Identify the preparation type.
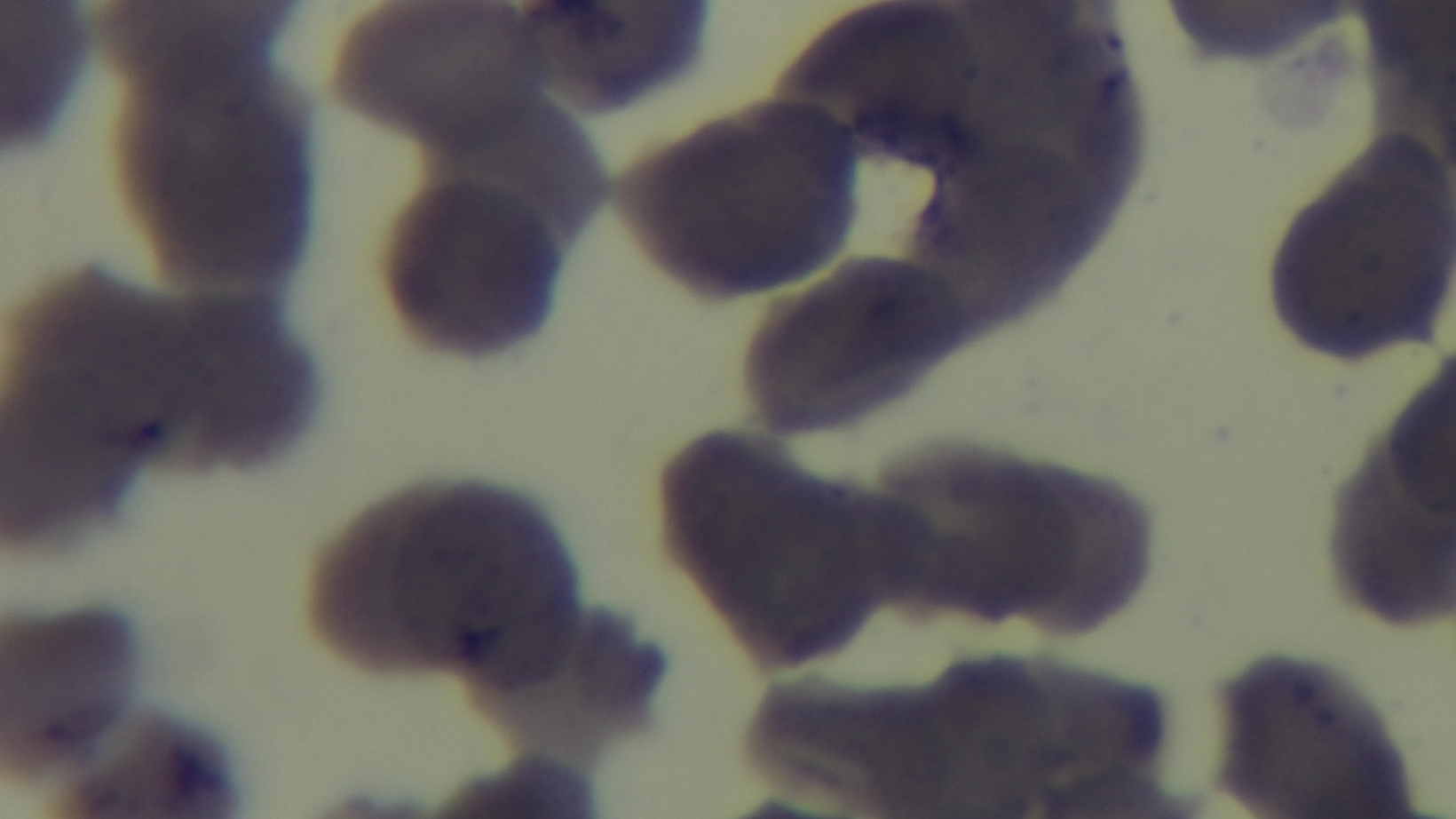
It is a thin blood film.

Single field of view. Light microscopy. Malaria status: uninfected. 100x oil-immersion objective. Giemsa-stained. Mounted 4K digital camera.